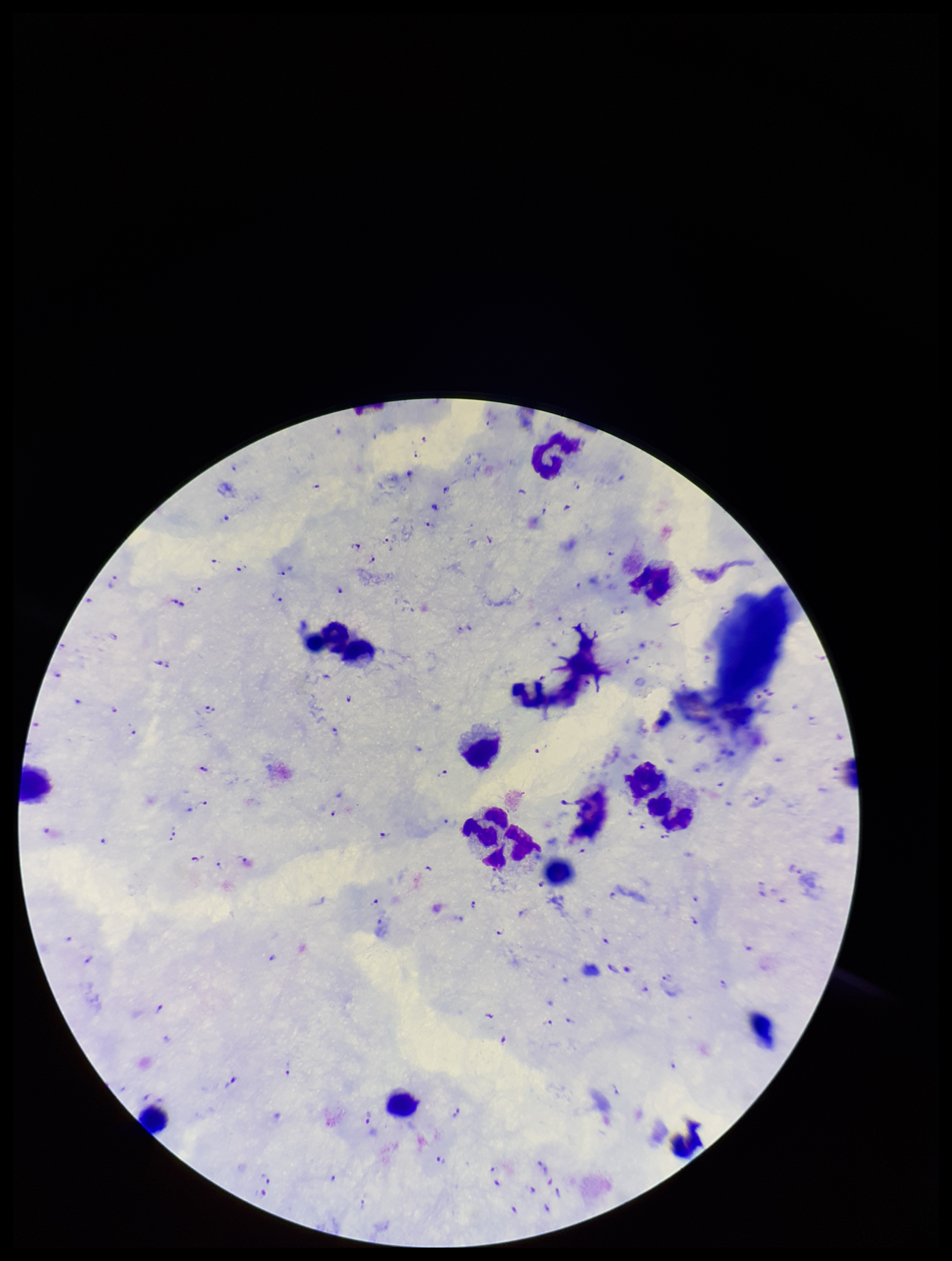

Summary:
  - Capture: smartphone photograph through the microscope eyepiece
  - Leukocyte count: 16
  - Preparation: thick smear
  - Stain: Giemsa
  - Species reported for this patient: Plasmodium falciparum
  - Field of view: single
  - Image size: 952×1261 pixels
  - Plasmodium parasites: detected
  - Parasite count: 107
  - Patient malaria status: infected